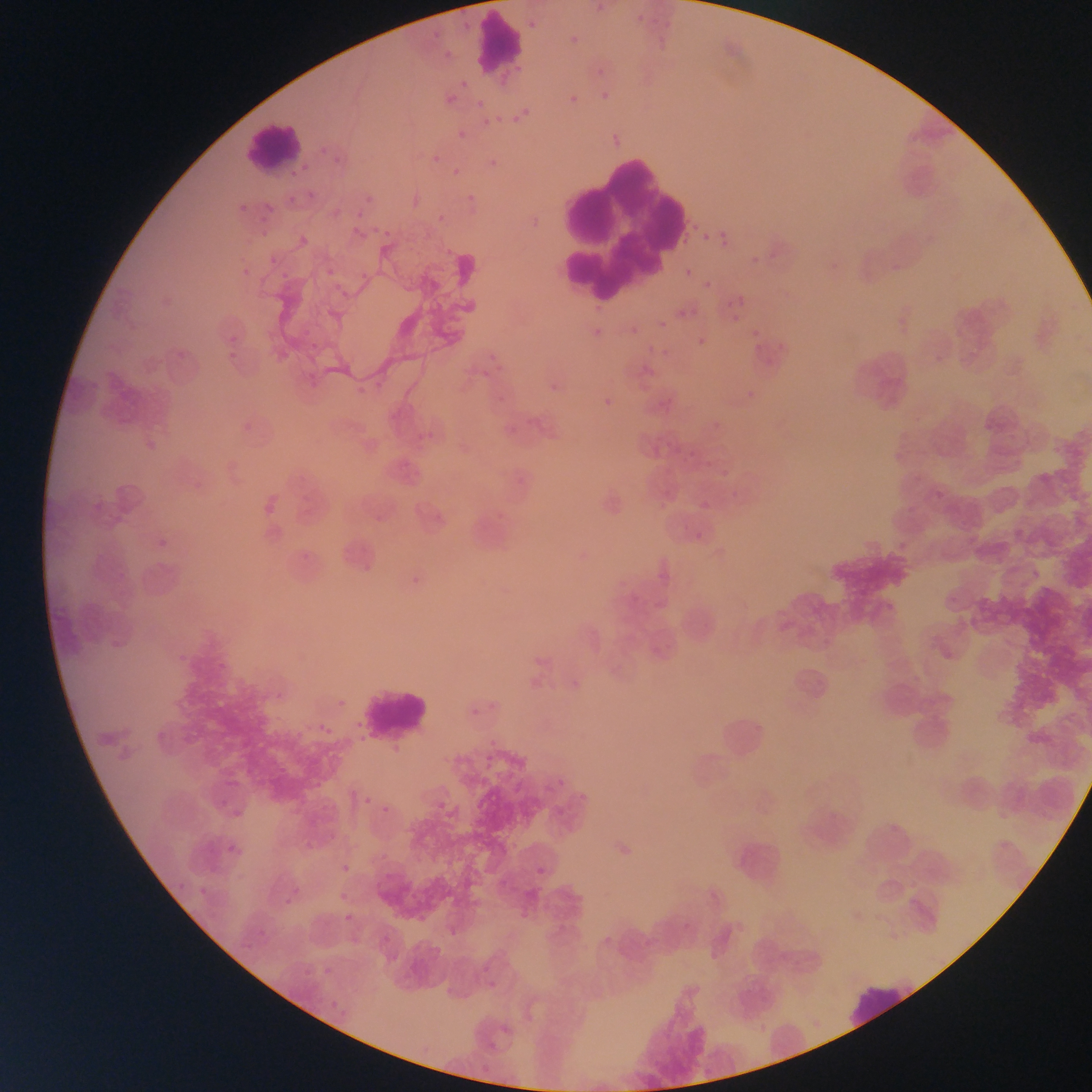
Approximate bounding boxes as [left, top, right, bottom] in pixels.
Summary:
  - Plasmodium parasite locations: [637, 15, 645, 22], [528, 20, 537, 29], [596, 87, 614, 104], [440, 93, 460, 102], [562, 93, 578, 107], [476, 99, 485, 109], [520, 103, 536, 117], [509, 115, 525, 126], [477, 118, 501, 131], [452, 129, 471, 142], [484, 151, 501, 172], [425, 153, 441, 163], [449, 173, 459, 179], [463, 191, 481, 202], [246, 201, 289, 245], [438, 213, 444, 221], [718, 222, 730, 243], [352, 227, 361, 235], [382, 229, 390, 238], [702, 233, 710, 241], [317, 262, 346, 282], [685, 267, 694, 276], [703, 281, 711, 290], [336, 283, 358, 301], [738, 296, 746, 305], [724, 300, 732, 308], [675, 309, 685, 318], [658, 320, 667, 329], [627, 327, 643, 334], [752, 329, 759, 337], [697, 337, 706, 347], [754, 342, 763, 351], [484, 370, 490, 378], [650, 395, 671, 411], [603, 398, 617, 407], [983, 421, 993, 430], [507, 426, 516, 434], [682, 449, 713, 471], [715, 466, 737, 479], [996, 466, 1004, 474], [518, 477, 526, 485], [259, 491, 295, 514], [699, 500, 709, 510], [374, 513, 383, 522], [695, 532, 704, 540], [569, 666, 591, 684], [477, 752, 503, 771], [361, 792, 374, 808], [434, 797, 450, 816], [380, 803, 391, 815], [339, 864, 350, 874], [533, 865, 549, 877], [340, 893, 349, 901], [344, 913, 353, 922], [500, 1024, 511, 1035], [489, 1042, 497, 1053] | approximate [x, y] pixel centers of objects too small to bound: [314, 346]
  - Leukocyte locations: [474, 11, 525, 76], [243, 121, 305, 171], [528, 152, 699, 304], [354, 683, 434, 745], [845, 983, 920, 1025]
  - Image size: 1092×1092 pixels
  - Field of view: single
  - Country: Ghana
  - Preparation: thin blood smear
  - Capture: mobile-phone photograph through a microscope